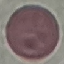
Summary:
  - Malaria status: uninfected
  - Capture: smartphone camera at the microscope eyepiece
  - Stain: Giemsa
  - Preparation: thin smear
  - Image type: cell patch, automatically extracted from a larger field of view and resized to 64 × 64 pixels